Locate and identify every blood parasite.
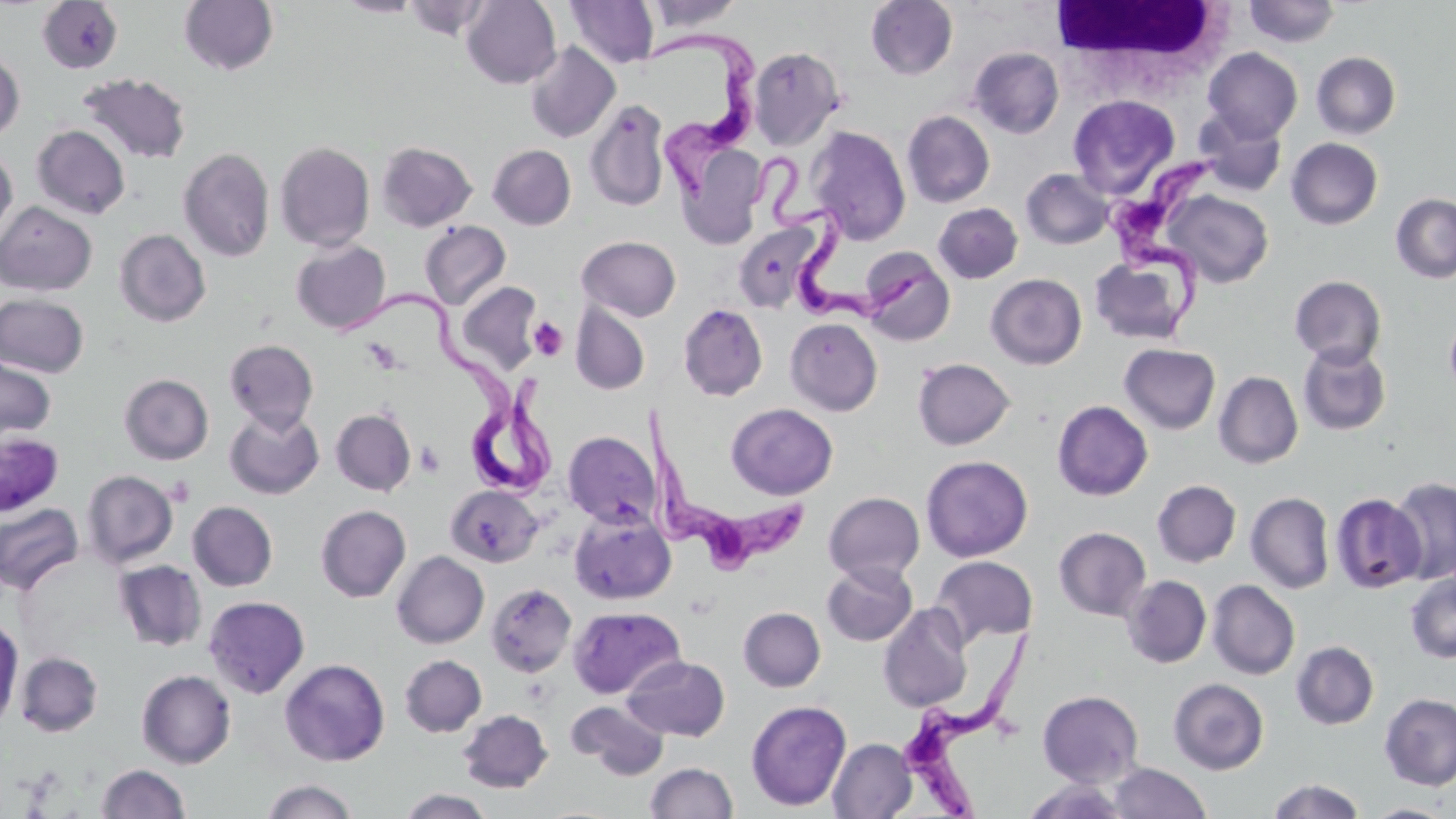
Approximate bounding boxes as (x1,y1)-(x2,y2) corner pairs in pixels.
Trypanosoma brucei: (641,31)-(761,204), (756,149)-(938,325), (1105,151)-(1221,340), (339,286)-(560,497), (639,405)-(807,578), (905,629)-(1036,818).
No Plasmodium falciparum, Plasmodium ovale, Plasmodium malariae, Plasmodium vivax, or Babesia divergens observed.

Uninfected red blood cell locations: (179,0)-(279,76), (336,0)-(424,17), (403,0)-(496,41), (462,0)-(561,88), (866,0)-(958,80), (1244,0)-(1341,47), (36,1)-(124,73), (566,1)-(659,69), (643,1)-(744,33), (524,42)-(620,143), (748,45)-(846,149), (968,46)-(1064,138), (1203,47)-(1303,143), (0,50)-(25,142), (1311,51)-(1401,139), (78,72)-(192,164), (1067,94)-(1179,197), (585,99)-(671,212), (902,110)-(995,208), (1194,110)-(1288,197), (32,125)-(131,219), (807,125)-(911,245), (1287,138)-(1383,230), (274,141)-(375,252), (376,142)-(477,231), (676,142)-(768,248), (487,144)-(576,229), (0,146)-(17,243), (178,147)-(275,262), (1020,168)-(1115,250), (1163,190)-(1274,288), (1391,193)-(1456,283), (0,201)-(97,296), (933,202)-(1023,284), (420,221)-(510,309), (733,222)-(821,312), (114,229)-(211,327), (576,235)-(682,321), (291,239)-(391,334), (860,247)-(956,346), (1089,253)-(1196,345), (986,274)-(1086,369), (1289,275)-(1387,369), (456,281)-(544,374), (0,294)-(89,377), (571,302)-(650,395), (678,303)-(768,401), (785,317)-(883,415), (1444,317)-(1456,397), (224,338)-(319,432), (1119,343)-(1221,433), (1297,343)-(1391,436), (0,356)-(56,443), (912,358)-(1015,450), (1214,371)-(1303,469), (120,373)-(214,465), (1052,400)-(1153,501), (726,403)-(838,500), (225,408)-(324,499), (330,408)-(416,496), (0,431)-(64,516), (562,431)-(660,528), (921,454)-(1033,562), (82,470)-(178,568), (1388,476)-(1456,585), (1152,480)-(1241,568), (446,485)-(543,568), (823,491)-(925,584), (1246,491)-(1335,594), (1329,492)-(1426,593), (0,501)-(84,595), (187,501)-(277,591), (316,505)-(411,602), (569,508)-(676,605), (1054,526)-(1151,620), (392,551)-(489,648), (931,555)-(1038,647), (113,560)-(207,651), (822,561)-(917,646), (1405,572)-(1456,663), (1122,575)-(1212,668), (1207,580)-(1300,680), (486,583)-(577,677), (203,595)-(310,698), (878,602)-(974,712), (568,605)-(685,699), (738,606)-(826,691), (0,619)-(23,728), (1291,641)-(1379,730), (16,651)-(103,736), (399,654)-(487,737), (622,655)-(730,741), (279,658)-(390,766), (137,669)-(236,768), (1168,677)-(1269,774), (1037,690)-(1144,787), (1379,693)-(1456,790), (746,699)-(852,811), (568,700)-(670,779), (458,709)-(553,793), (828,737)-(917,818), (645,762)-(738,819), (1108,762)-(1212,819), (96,763)-(190,818), (1266,777)-(1366,819), (259,778)-(359,819), (1021,778)-(1131,819), (397,788)-(495,818), (1363,802)-(1453,818). White blood cell locations: (1050,1)-(1238,88). Platelet locations: (528,317)-(569,361), (415,440)-(445,476). Slide-level diagnosis: Trypanosoma brucei. Image is 1456×819 pixels. Captured at 1000x magnification. Single field of view. Light microscopy. May-Grünwald-Giemsa stain. Thin blood smear.